Describe the morphology of the red blood cells.
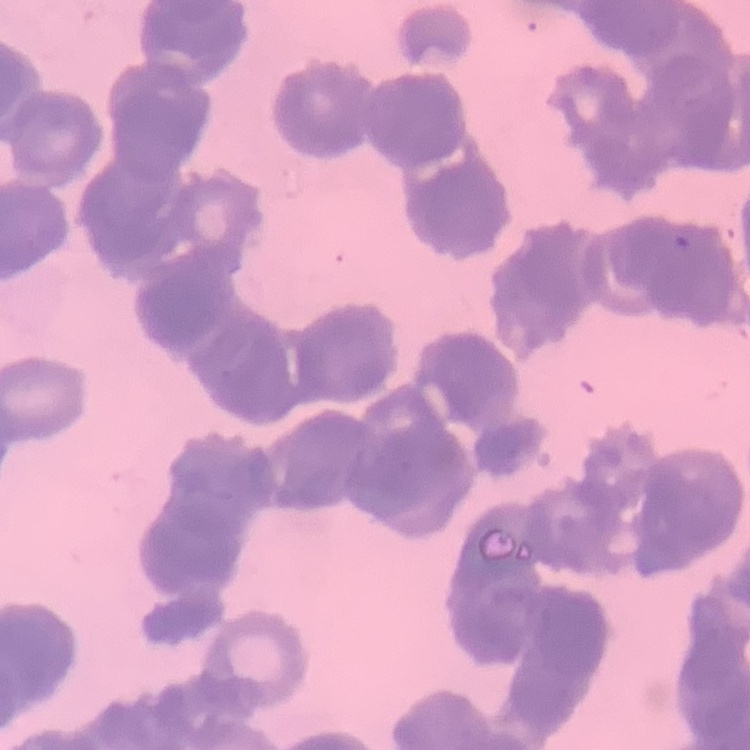

They show rouleaux formation.

Summary:
  - Image type: square crop of a larger photomicrograph
  - Preparation: thin peripheral smear
  - Stain: Field's or Giemsa